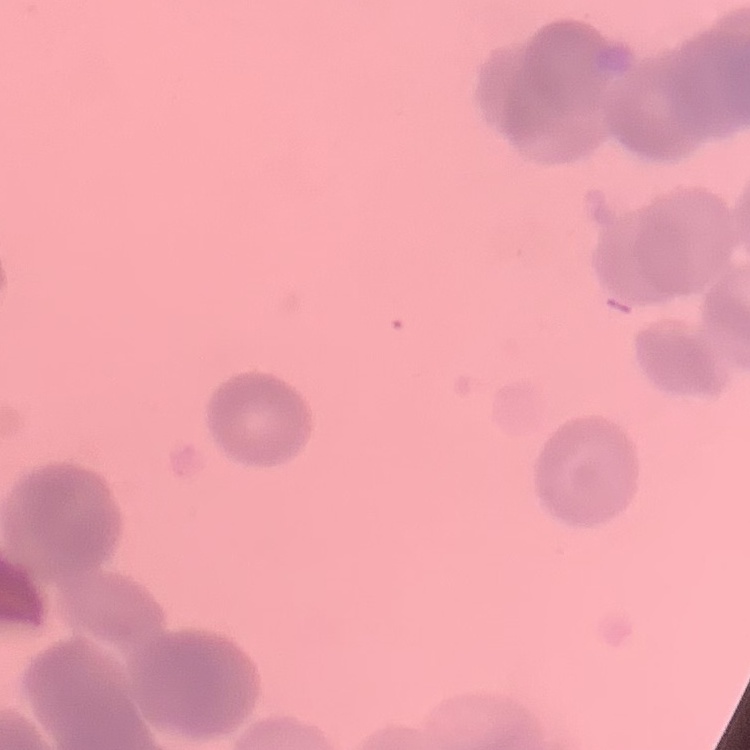
Summary:
  - Erythrocyte morphology: rouleaux formation
  - Stain: Field's or Giemsa
  - Preparation: thin blood film
  - Image type: one tile cut from a larger photomicrograph